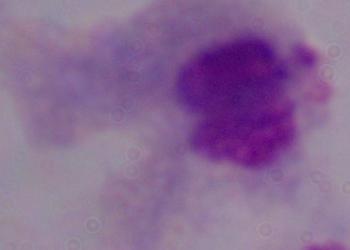
Summary:
  - Modality: micrograph
  - Magnification: 1000x
  - Identification: trichomonad